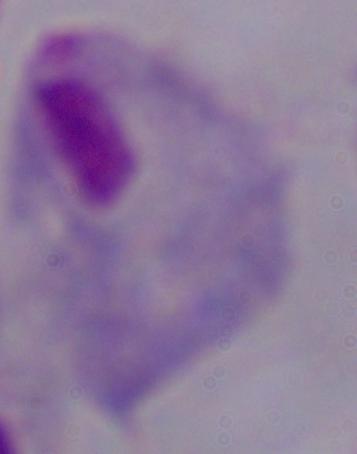
Summary:
  - Modality: micrograph
  - Magnification: 1000x
  - Identification: trichomonad